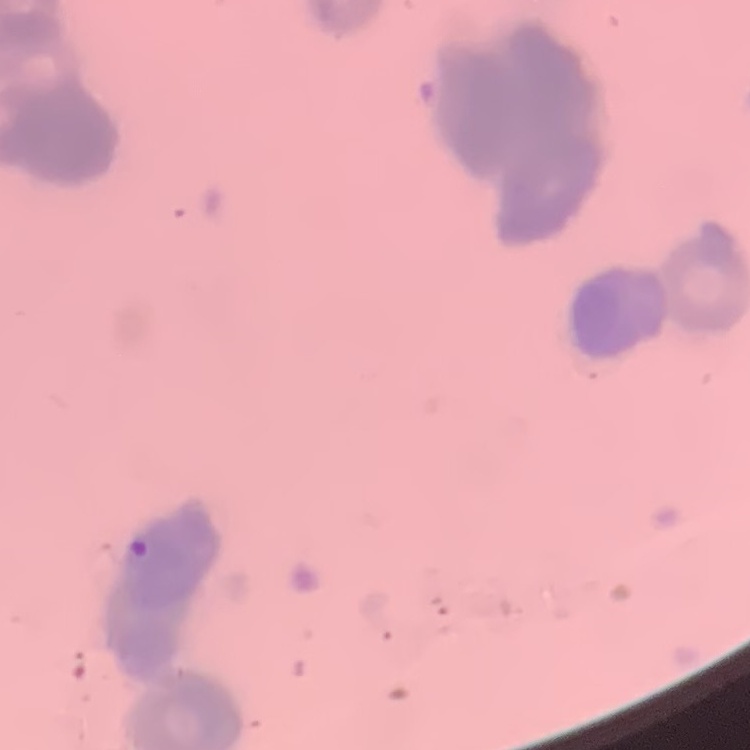
The red blood cells exhibit rouleaux formation. Stained with either Field's or Giemsa. Square crop of a larger photomicrograph. Thin peripheral smear.